Point out each malaria parasite.
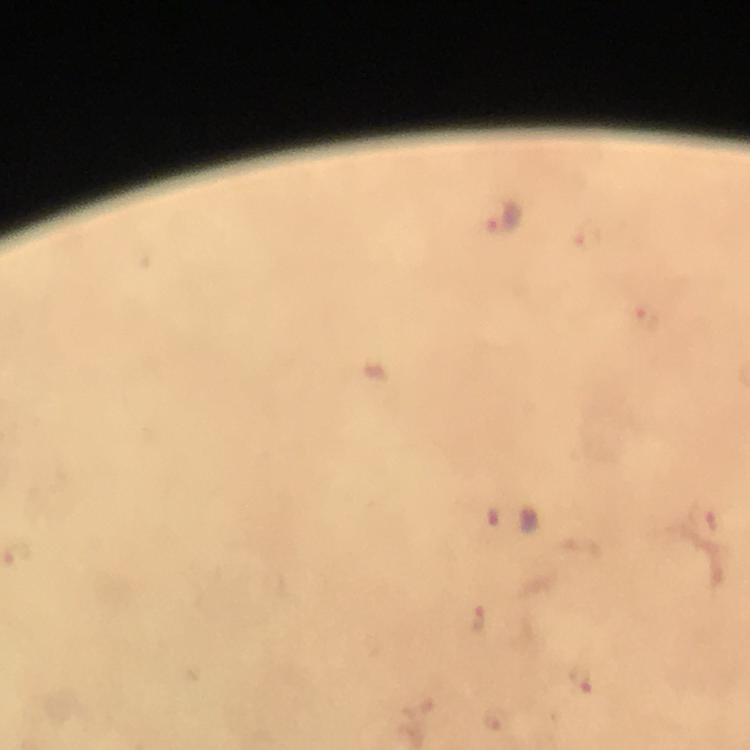
Approximate centers as {x, y} in pixels.
Malaria parasites: {502, 215}, {588, 236}, {646, 319}, {513, 517}, {477, 617}, {582, 677}.

capture: smartphone photograph through a microscope
preparation: thick blood smear
context: from a diagnostic examination for malaria
magnification: 100x
cropped_from: one field of view
immersion_oil: used
stain: Giemsa
image_size: 750×750 pixels